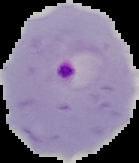
Summary:
  - Preparation: thin blood smear
  - Malaria status: parasitized
  - Image size: 139×163 pixels
  - Image type: cell region segmented out of the field of view; surrounding area masked to black